Give the extent of all Plasmodium malariae-infected red blood cells.
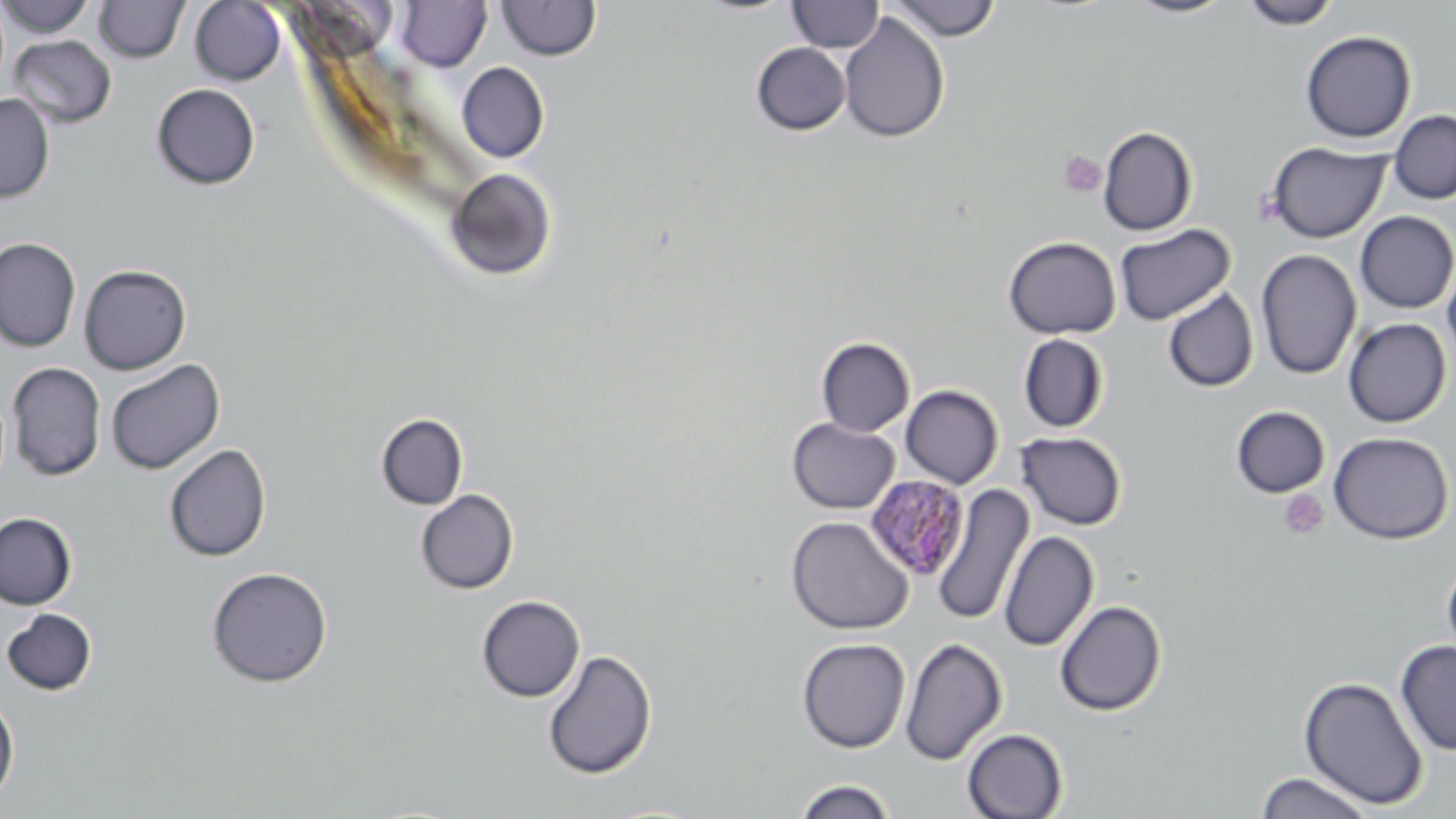
Approximate bounding boxes as (x1, y1, x2, y2) in pixels.
Plasmodium malariae-infected red blood cells: (864, 474, 971, 582).

{
  "slide_level_diagnosis": "Plasmodium malariae",
  "platelet_locations": "approximate bounding boxes as (x1, y1, x2, y2) in pixels: (1057, 151, 1106, 198), (1279, 491, 1328, 541)",
  "modality": "optical microscopy",
  "uninfected_red_blood_cell_locations": "approximate bounding boxes as (x1, y1, x2, y2) in pixels: (1, 0, 96, 38), (787, 0, 884, 52), (1125, 0, 1237, 19), (1239, 0, 1342, 30), (94, 1, 189, 63), (189, 1, 286, 85), (395, 1, 492, 71), (498, 1, 601, 61), (886, 1, 1002, 41), (838, 12, 950, 144), (1300, 30, 1416, 143), (8, 35, 117, 127), (751, 42, 851, 135), (456, 62, 549, 163), (152, 83, 260, 190), (0, 93, 55, 203), (1388, 109, 1456, 205), (1098, 127, 1197, 235), (1266, 141, 1391, 242), (446, 167, 557, 281), (1355, 211, 1456, 313), (1114, 224, 1235, 325), (1002, 236, 1121, 339), (0, 237, 81, 352), (1256, 249, 1361, 381), (1441, 257, 1456, 372), (79, 263, 191, 375), (1162, 287, 1258, 394), (1343, 317, 1452, 427), (1019, 334, 1109, 433), (816, 336, 915, 436), (105, 358, 225, 475), (7, 362, 106, 481), (900, 385, 1003, 488), (1230, 405, 1330, 498), (376, 413, 468, 510), (787, 418, 899, 513), (1015, 432, 1127, 531), (1328, 432, 1454, 544), (164, 443, 272, 563), (931, 485, 1033, 627), (415, 489, 519, 594), (0, 512, 77, 609), (786, 515, 914, 635), (999, 530, 1098, 652), (1441, 555, 1456, 668), (206, 567, 333, 688), (477, 594, 585, 702), (1054, 599, 1166, 716), (1, 608, 97, 696), (797, 637, 910, 753), (900, 637, 1007, 765), (1396, 639, 1456, 756), (542, 648, 657, 780), (1299, 675, 1428, 808), (0, 694, 19, 806), (962, 728, 1068, 818), (1255, 771, 1376, 818), (793, 778, 897, 819)",
  "preparation": "thin blood film",
  "image_size": "1456×819 pixels",
  "stain": "May-Grünwald-Giemsa",
  "field_of_view": "single",
  "magnification": "1000x"
}